Describe the morphology of the red blood cells.
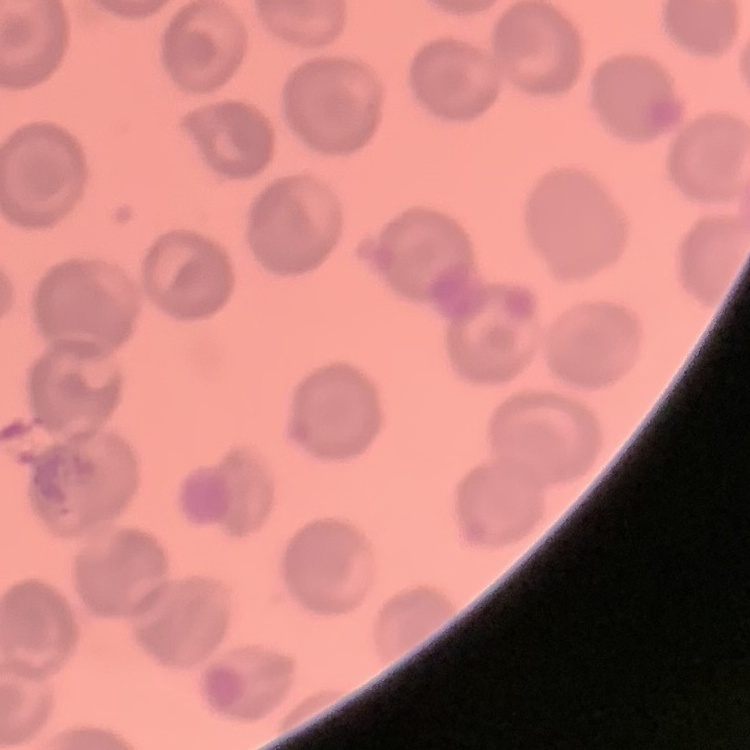
No rouleaux formation.

Summary:
  - Stain: Field's or Giemsa
  - Preparation: thin blood smear
  - Image type: one tile cut from a larger photomicrograph